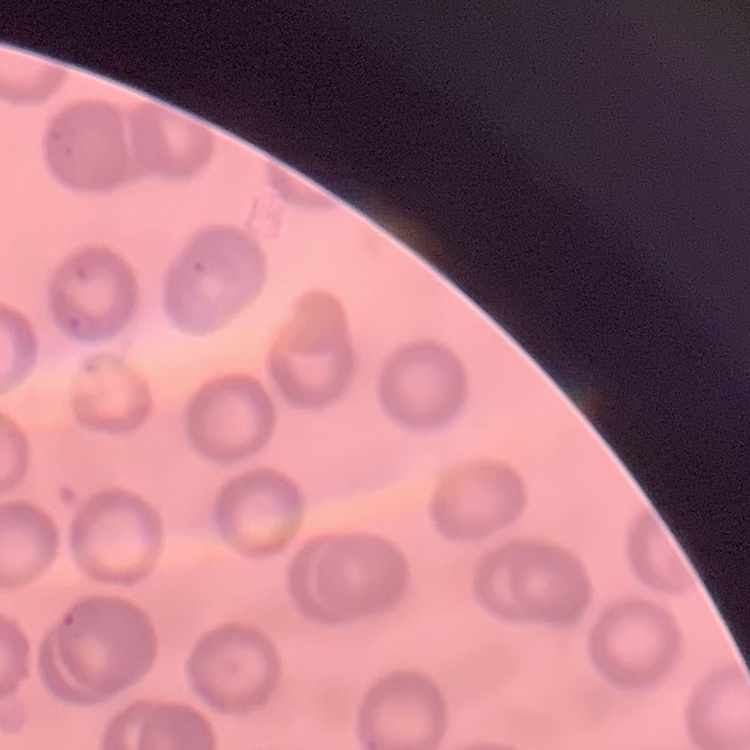

Summary:
  - Erythrocyte morphology: no rouleaux formation
  - Stain: Field's or Giemsa
  - Preparation: thin peripheral smear
  - Image type: one tile cut from a larger photomicrograph